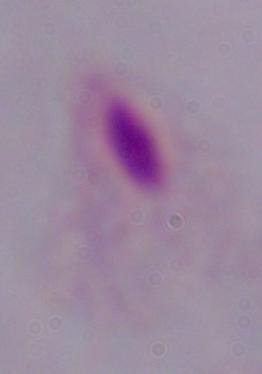
Summary:
  - Modality: photomicrograph
  - Identification: trichomonad
  - Magnification: 1000x